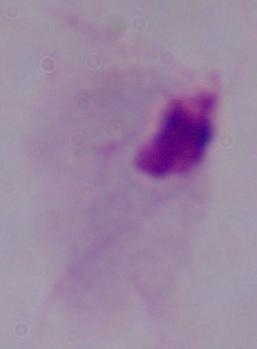
identification = trichomonad
magnification = 1000x
modality = photomicrograph